Assess this cell for malaria.
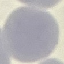

It is uninfected.

Summary:
  - Preparation: thin blood film
  - Stain: Giemsa
  - Capture: smartphone through the microscope eyepiece
  - Image type: automatically extracted cell patch, resized to 64 × 64 pixels